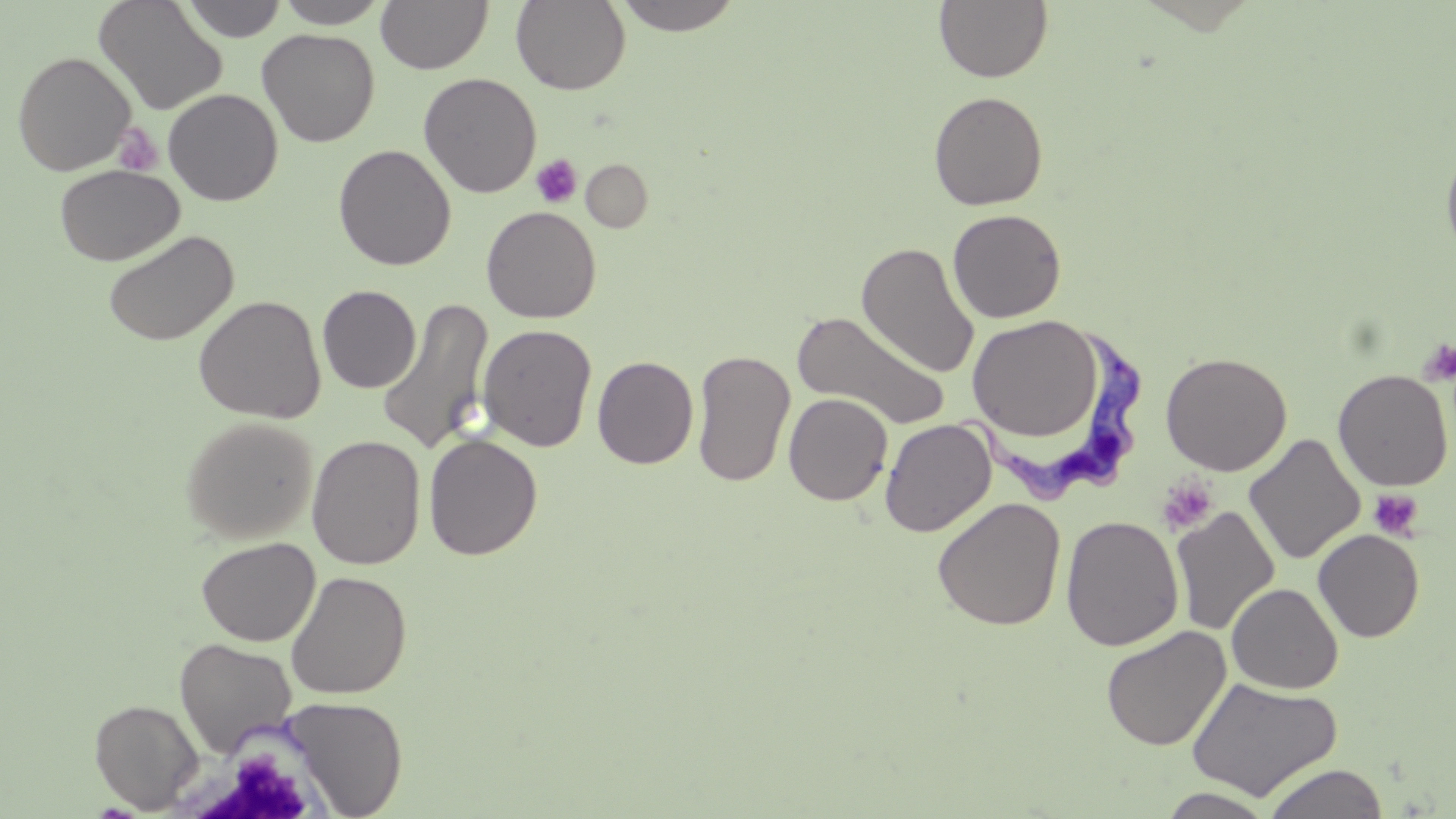

Summary:
  - Coordinate format: approximate bounding boxes as (x1,y1)-(x2,y2) corner pairs in pixels
  - Uninfected red blood cell locations: (93,0)-(227,115), (181,0)-(288,42), (274,0)-(391,28), (375,0)-(492,74), (511,0)-(631,94), (612,0)-(745,35), (934,0)-(1054,83), (257,28)-(380,147), (12,51)-(137,176), (418,72)-(542,198), (163,88)-(284,206), (928,90)-(1048,211), (1440,138)-(1456,266), (333,143)-(456,270), (581,159)-(653,232), (54,164)-(185,266), (481,206)-(602,324), (947,209)-(1067,323), (102,229)-(238,347), (857,242)-(979,379), (317,285)-(421,393), (193,295)-(327,423), (377,298)-(494,456), (792,310)-(951,430), (965,315)-(1105,441), (477,323)-(597,452), (691,349)-(795,487), (1160,351)-(1292,475), (592,356)-(698,468), (1332,370)-(1453,491), (783,392)-(893,506), (180,415)-(319,543), (879,418)-(997,537), (423,432)-(543,560), (306,434)-(426,570), (1244,434)-(1365,565), (932,497)-(1066,631), (1170,507)-(1280,636), (1061,515)-(1184,651), (1313,529)-(1424,642), (196,536)-(320,646), (285,570)-(412,699), (1227,582)-(1343,694), (1101,625)-(1231,751), (174,637)-(297,757), (1185,676)-(1343,802), (282,696)-(408,817), (90,698)-(202,813), (1262,762)-(1390,819), (1158,788)-(1276,818)
  - Platelet locations: (114,123)-(164,178), (530,155)-(582,208), (1418,339)-(1456,386), (1156,475)-(1219,536), (1367,489)-(1423,541)
  - Trypanosoma brucei locations: (957,319)-(1150,513)
  - Slide-level diagnosis: Trypanosoma brucei
  - Image size: 1456×819 pixels
  - Preparation: thin blood film
  - Modality: light microscopy
  - Stain: May-Grünwald-Giemsa
  - Magnification: 1000x
  - Field of view: one of a larger specimen